Assess this cell for malaria.
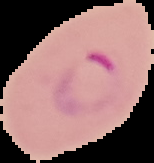
Parasitized.

{
  "image_size": "154×163 pixels",
  "preparation": "thin blood smear",
  "image_type": "segmented cell region with the area outside set to black"
}